Outline each blood parasite and name the species.
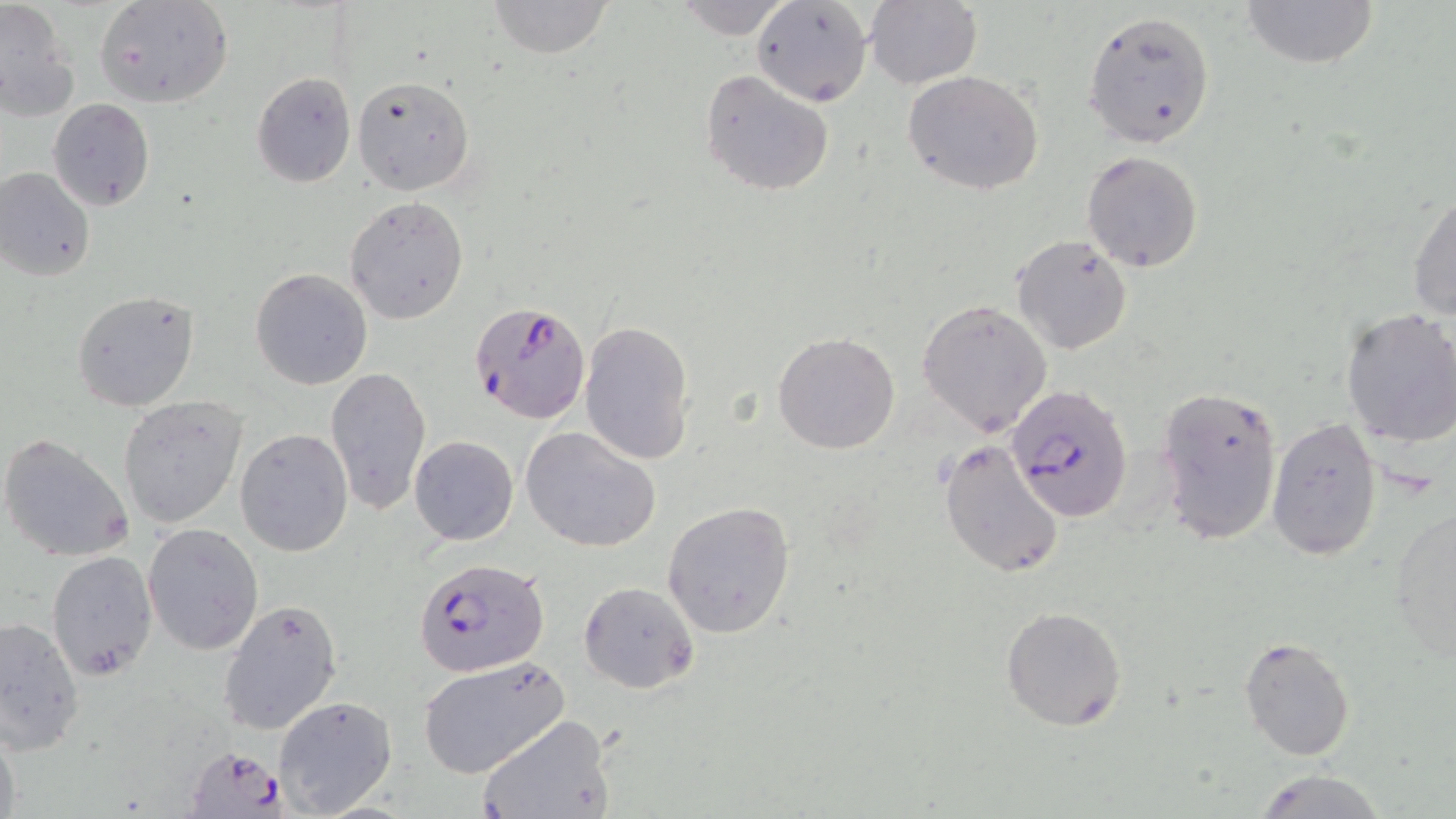
Approximate bounding boxes as [x1, y1, x2, y2] in pixels.
Plasmodium falciparum-infected red blood cells: [469, 300, 589, 424], [1007, 383, 1132, 521], [413, 557, 549, 679], [189, 748, 292, 819].
No Plasmodium ovale, Plasmodium malariae, Plasmodium vivax, Babesia divergens, or Trypanosoma brucei observed.

slide_level_diagnosis: Plasmodium falciparum
preparation: thin blood film
field_of_view: single
magnification: 1000x
modality: light microscopy
image_size: 1456×819 pixels
stain: May-Grünwald-Giemsa
uninfected_red_blood_cell_locations: 'approximate bounding boxes as [x1, y1, x2, y2] in pixels: [1, 0, 77, 120], [95, 0, 234, 110], [486, 0, 615, 59], [752, 0, 875, 105], [1239, 0, 1378, 70], [864, 1, 982, 89], [1082, 11, 1216, 148], [902, 70, 1044, 196], [252, 72, 356, 186], [700, 72, 834, 197], [354, 75, 476, 195], [47, 99, 156, 211], [1081, 150, 1204, 272], [0, 166, 96, 282], [1408, 189, 1455, 324], [345, 197, 469, 324], [1011, 234, 1132, 355], [250, 268, 374, 391], [70, 290, 199, 412], [917, 298, 1053, 436], [1339, 307, 1456, 449], [580, 320, 695, 464], [772, 333, 900, 454], [323, 366, 430, 515], [1154, 383, 1284, 547], [118, 395, 248, 529], [1265, 417, 1382, 561], [521, 426, 661, 552], [236, 428, 353, 557], [0, 432, 135, 565], [410, 436, 518, 545], [939, 438, 1066, 579], [662, 500, 796, 638], [1389, 507, 1456, 660], [143, 524, 264, 655], [46, 549, 157, 681], [579, 582, 699, 694], [218, 598, 343, 735], [1000, 607, 1128, 732], [2, 615, 86, 755], [1238, 633, 1357, 760], [418, 656, 570, 777], [273, 695, 397, 816], [476, 714, 615, 819], [0, 716, 23, 819], [1249, 771, 1388, 819]'